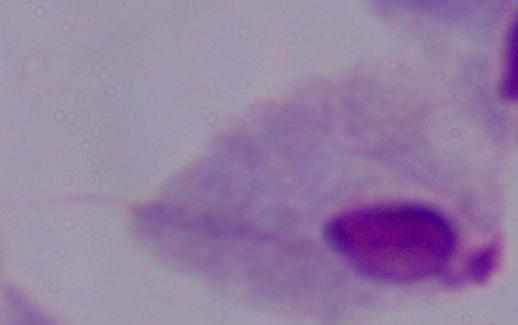
Summary:
  - Modality: photomicrograph
  - Magnification: 1000x
  - Identification: trichomonad